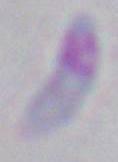

Summary:
  - Magnification: 1000x
  - Modality: micrograph
  - Identification: Toxoplasma gondii